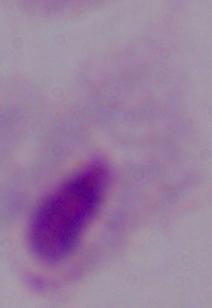

Summary:
  - Identification: trichomonad
  - Modality: micrograph
  - Magnification: 1000x